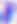
Photomicrograph. 400x magnification. Toxoplasma gondii is shown.